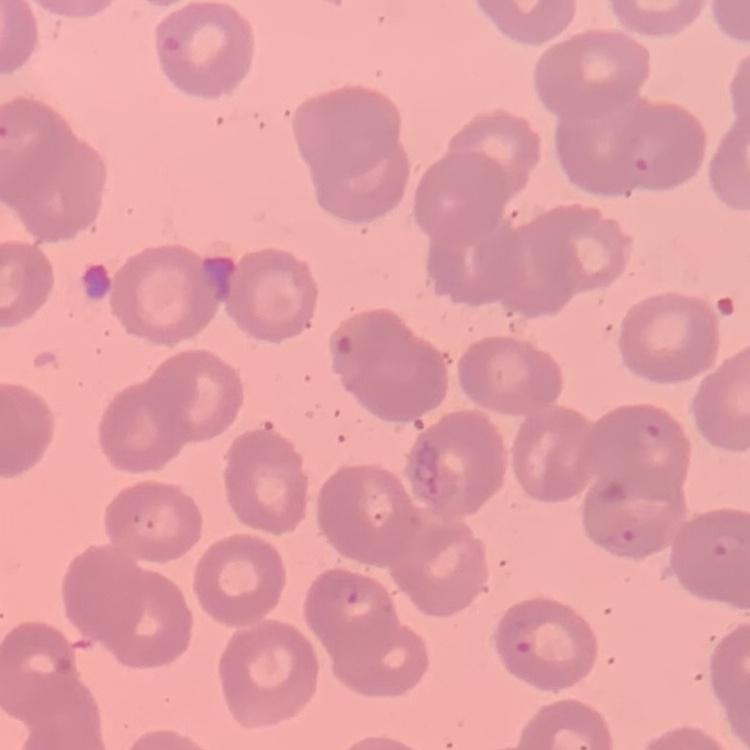
The red blood cells show no rouleaux formation. Stained with either Field's or Giemsa. Thin peripheral smear. One tile cut from a larger photomicrograph.